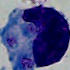
Summary:
  - Modality: micrograph
  - Magnification: 1000x
  - Identification: white blood cell